Assess the morphology of the red blood cells.
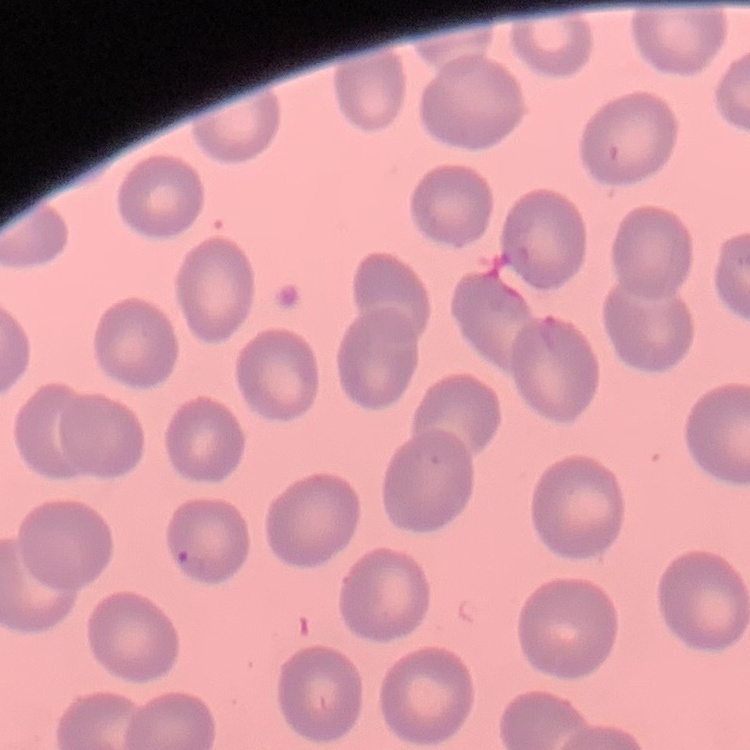
They show no rouleaux formation.

image type = square crop of a larger photomicrograph
preparation = thin blood smear
stain = Field's or Giemsa